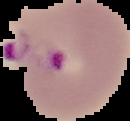

Image is 130×121 pixels. Malaria status: parasitized. From a thin blood smear. The area outside the segmented cell region is set to black.